Report the malaria status of this cell.
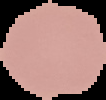
Uninfected.

Segmented cell region on a black background. From a thin blood smear. Image is 106×100 pixels.